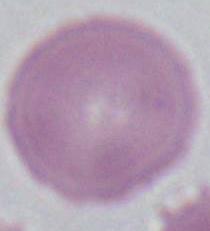

Summary:
  - Magnification: 1000x
  - Modality: micrograph
  - Identification: erythrocyte